Give the extent of all Plasmodium vivax-infected red blood cells.
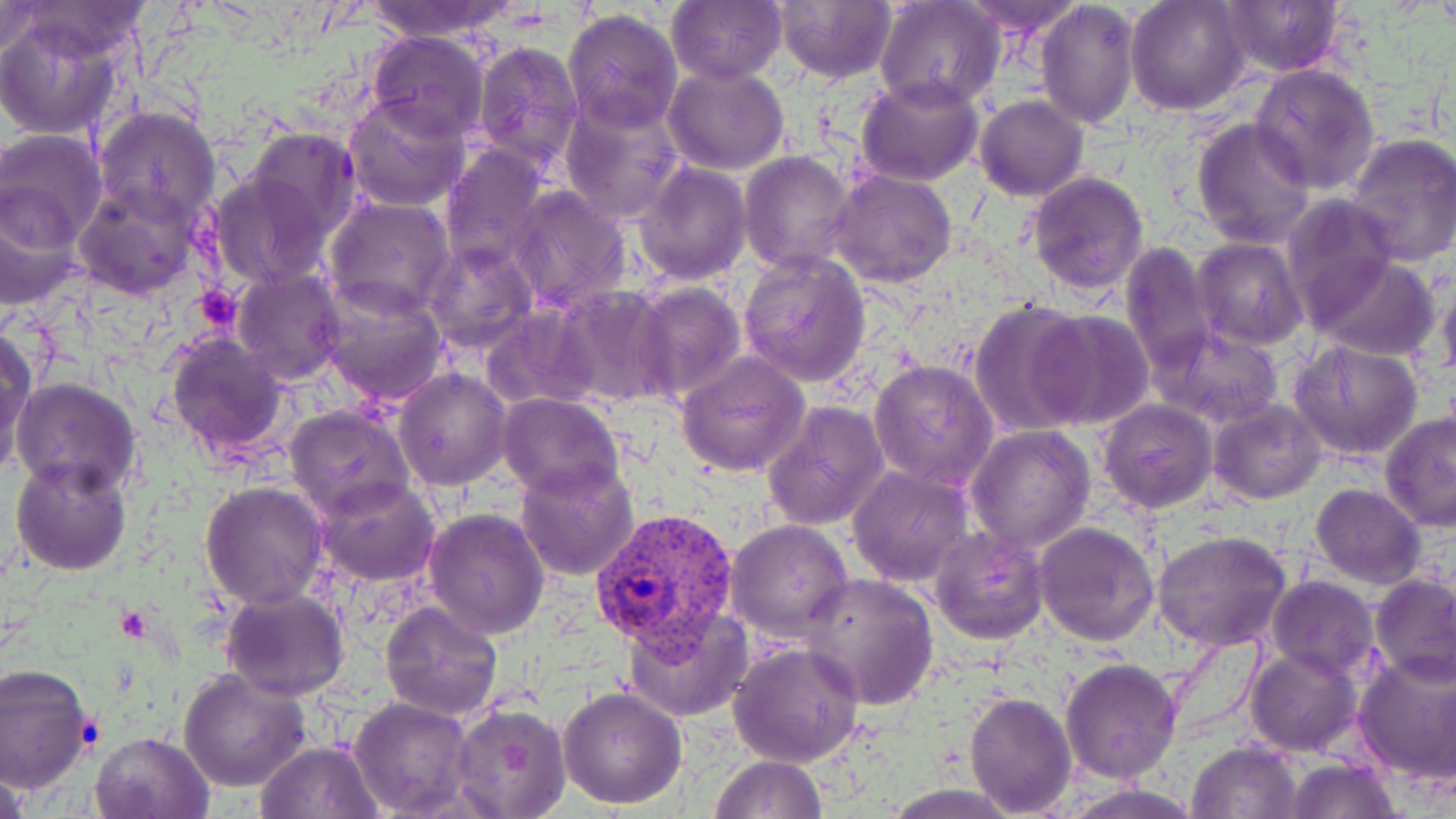
Approximate bounding boxes as (x1, y1, x2, y2) in pixels.
Plasmodium vivax-infected red blood cells: (591, 506, 740, 670).

Platelet locations: (192, 285, 242, 334), (117, 604, 150, 639). Uninfected red blood cell locations: (361, 0, 519, 42), (772, 0, 897, 85), (956, 0, 1085, 36), (1126, 0, 1250, 115), (666, 1, 786, 85), (1036, 1, 1139, 131), (874, 2, 1005, 113), (1218, 2, 1346, 77), (13, 3, 156, 63), (0, 4, 49, 60), (562, 7, 684, 134), (0, 13, 127, 142), (366, 32, 490, 139), (470, 41, 585, 175), (663, 62, 790, 175), (1249, 65, 1381, 195), (855, 75, 984, 185), (343, 92, 471, 211), (558, 94, 686, 223), (974, 95, 1088, 200), (93, 104, 221, 227), (1191, 116, 1313, 248), (244, 125, 363, 244), (0, 129, 107, 249), (1342, 133, 1456, 266), (439, 144, 551, 275), (739, 151, 856, 273), (634, 160, 752, 284), (829, 168, 957, 288), (206, 171, 332, 291), (1026, 171, 1148, 295), (75, 182, 205, 299), (508, 185, 632, 311), (0, 187, 83, 309), (325, 196, 456, 317), (1282, 198, 1400, 321), (1194, 238, 1305, 347), (425, 241, 538, 357), (1119, 242, 1216, 377), (739, 251, 872, 386), (1310, 255, 1440, 360), (231, 268, 345, 386), (1437, 277, 1456, 387), (319, 281, 450, 407), (629, 281, 746, 406), (550, 286, 672, 409), (969, 302, 1094, 435), (481, 304, 599, 412), (1031, 310, 1156, 431), (0, 326, 37, 478), (1157, 326, 1286, 429), (164, 331, 290, 460), (1291, 340, 1424, 463), (677, 350, 812, 478), (870, 359, 997, 490), (393, 367, 513, 491), (11, 378, 142, 497), (496, 392, 623, 499), (1099, 400, 1216, 511), (1209, 400, 1325, 503), (761, 401, 889, 533), (284, 405, 413, 519), (1379, 411, 1455, 532), (967, 425, 1095, 552), (9, 454, 133, 576), (515, 461, 640, 582), (848, 464, 975, 587), (312, 476, 439, 587), (199, 481, 329, 611), (1310, 483, 1425, 588), (423, 507, 549, 639), (725, 520, 853, 641), (1034, 521, 1160, 646), (930, 527, 1049, 644), (1152, 531, 1291, 651), (801, 571, 940, 709), (1371, 575, 1455, 684), (1266, 576, 1379, 681), (220, 586, 349, 699), (380, 600, 503, 720), (622, 605, 752, 721), (727, 642, 865, 768), (1244, 646, 1363, 757), (1354, 650, 1456, 787), (1061, 658, 1182, 783), (0, 664, 96, 795), (178, 667, 312, 793), (558, 686, 688, 809), (963, 690, 1078, 815), (348, 697, 474, 818), (449, 703, 572, 819), (90, 730, 216, 819), (254, 739, 383, 819), (1188, 741, 1304, 818), (710, 754, 828, 818), (1280, 757, 1402, 818), (0, 761, 32, 819). Slide-level diagnosis: Plasmodium vivax. Image is 1456×819 pixels. May-Grünwald-Giemsa-stained preparation. 1000x magnification. Single field of view. Thin blood film. Optical microscopy.